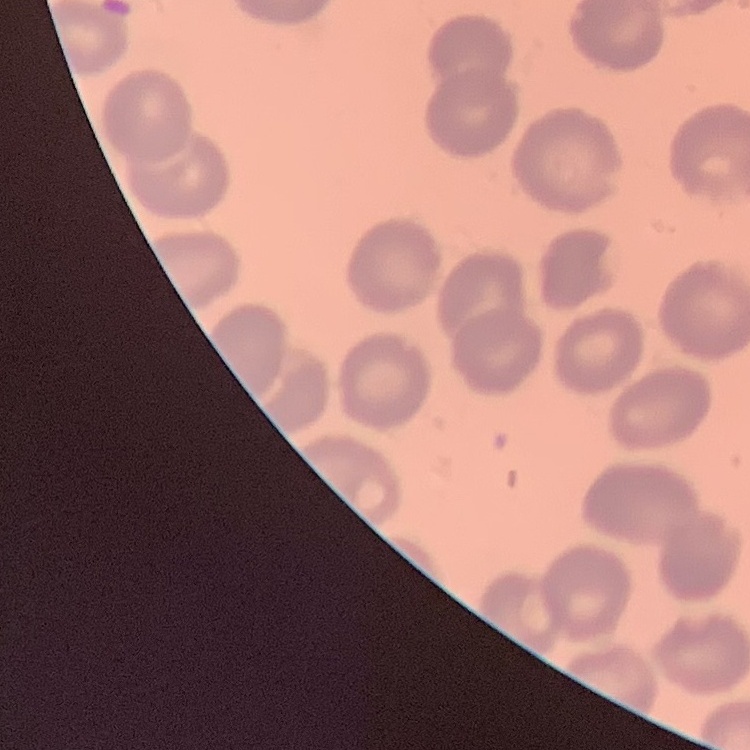

Summary:
  - Red blood cell morphology: no rouleaux formation
  - Preparation: thin blood smear
  - Stain: Field's or Giemsa
  - Image type: one tile cut from a larger photomicrograph